Report the malaria status of this cell.
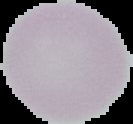

Uninfected.

Summary:
  - Image size: 133×124 pixels
  - Preparation: thin blood film
  - Image type: segmented cell region with the area outside set to black